Name the parasite shown.
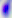
Toxoplasma gondii.

Summary:
  - Modality: photomicrograph
  - Magnification: 400x